Locate every Plasmodium falciparum parasite and identify its life-cycle stage.
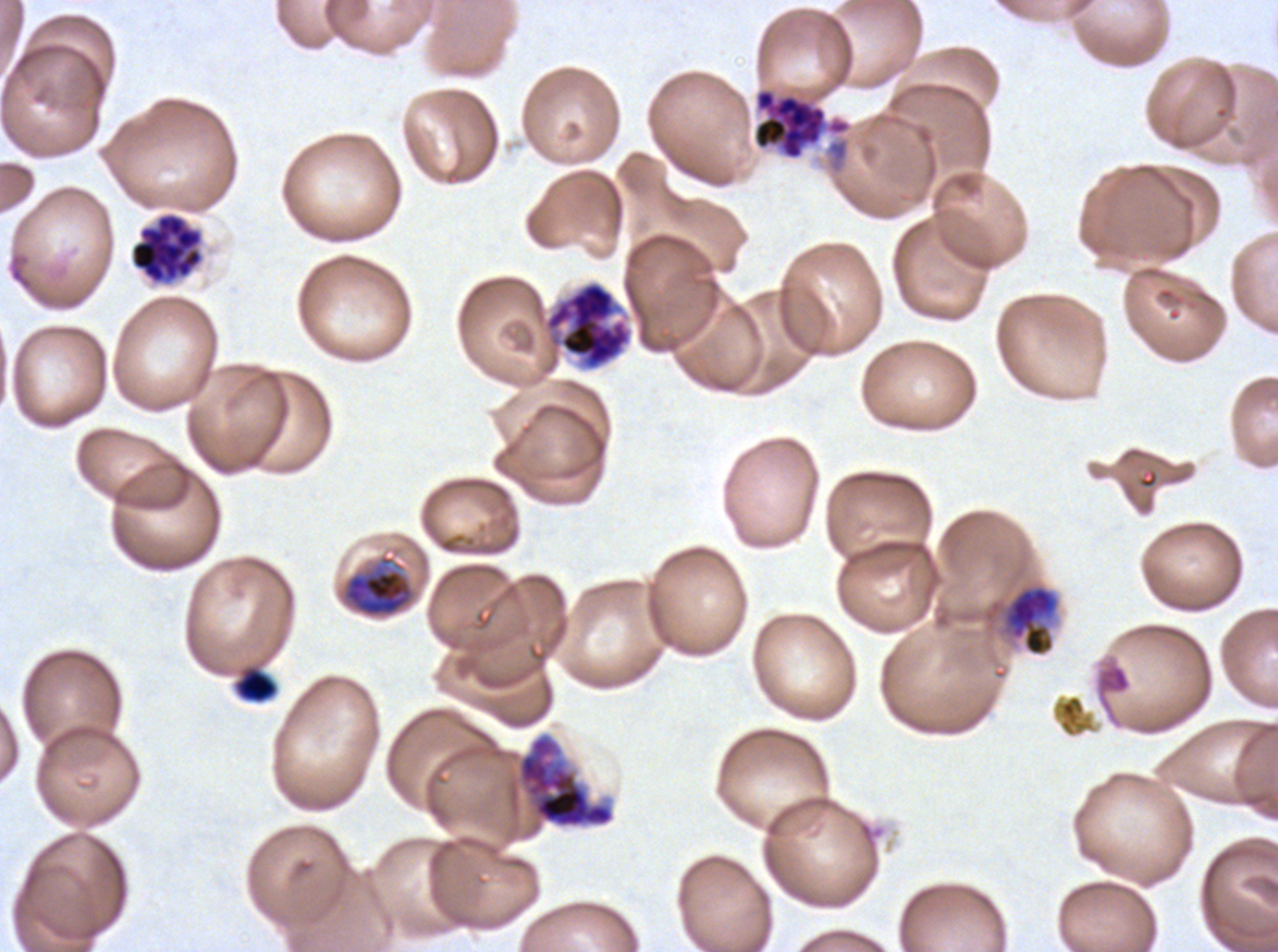

Approximate bounding boxes as [x1, y1, x2, y2] in pixels.
Late trophozoites: [340, 554, 415, 618], [1001, 584, 1060, 657].
Early schizonts: [517, 734, 615, 828].
Segmenters: [752, 88, 851, 161], [129, 212, 204, 285], [543, 280, 633, 371].
No rings, late-ring/early-trophozoite forms, mid trophozoites, late schizonts, or gametocytes observed.

debris locations = [1094, 659, 1132, 724], [235, 666, 277, 703]
life-cycle stages observed = late trophozoite, early schizont, segmenter
image size = 1278×952 pixels
preparation = thin blood film
specimen = Plasmodium falciparum cultured ex vivo for 24 to 48 hours, from a patient in The Gambia
field of view = one sub-image of a larger composite
stain = Giemsa